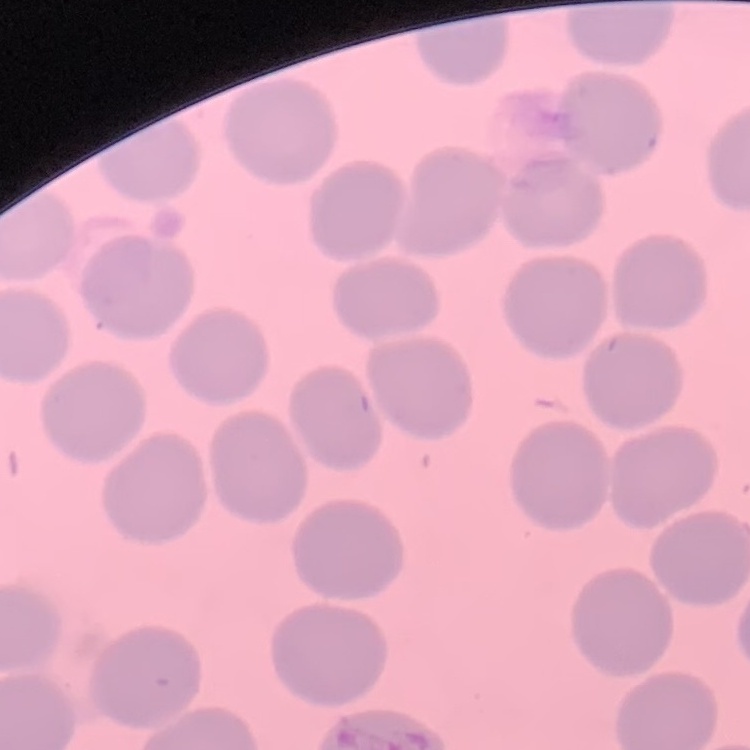
The red blood cells show no rouleaux formation. Thin blood film. Square crop of a larger photomicrograph. Field's or Giemsa stain.